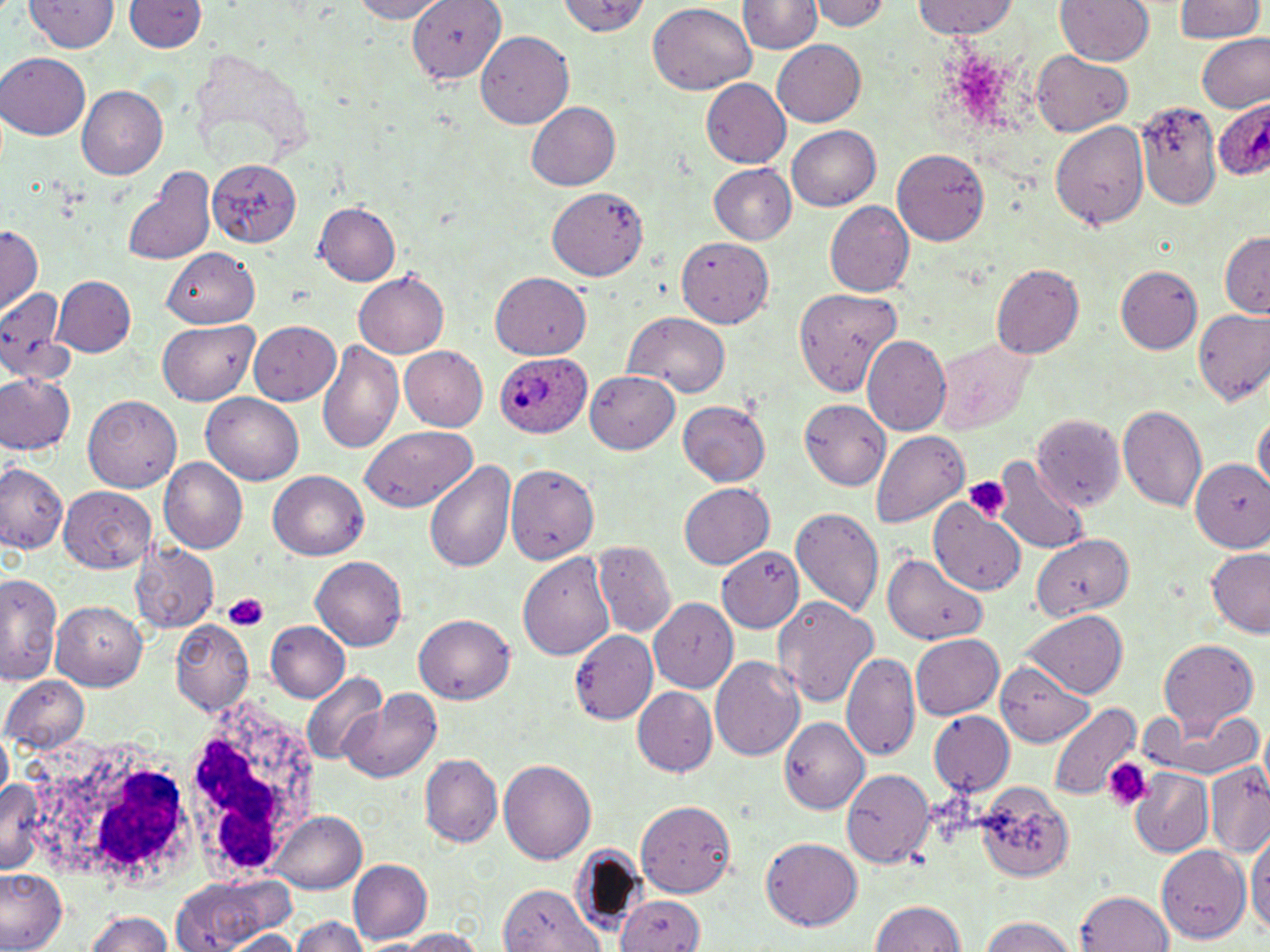

plasmodium_ovale_infected_red_blood_cell_locations: 'approximate bounding boxes as (x1, y1, x2, y2) in pixels: (1212, 99, 1270, 186), (486, 344, 590, 442)'
slide_level_diagnosis: Plasmodium ovale
magnification: 1000x
stain: May-Grünwald-Giemsa
preparation: thin blood film
uninfected_red_blood_cell_locations: 'approximate bounding boxes as (x1, y1, x2, y2) in pixels: (22, 0, 121, 54), (350, 0, 444, 22), (408, 0, 503, 82), (562, 0, 649, 41), (811, 0, 890, 30), (1055, 0, 1152, 66), (1172, 0, 1263, 43), (124, 1, 207, 55), (742, 1, 820, 56), (911, 1, 1024, 40), (1183, 2, 1263, 92), (645, 3, 757, 95), (480, 31, 575, 130), (1196, 34, 1270, 114), (771, 37, 867, 125), (1, 54, 90, 141), (1032, 54, 1132, 134), (702, 77, 791, 169), (77, 85, 167, 177), (1135, 100, 1223, 208), (526, 102, 620, 191), (1050, 118, 1151, 235), (785, 126, 881, 211), (893, 147, 991, 244), (209, 160, 301, 246), (123, 163, 218, 268), (707, 163, 797, 246), (551, 188, 646, 280), (825, 201, 913, 297), (314, 202, 401, 287), (0, 225, 42, 312), (1218, 231, 1270, 319), (676, 238, 776, 330), (164, 248, 258, 327), (992, 264, 1083, 360), (1117, 265, 1202, 357), (355, 270, 449, 356), (490, 274, 593, 359), (54, 275, 135, 354), (0, 286, 72, 380), (795, 288, 903, 398), (1191, 308, 1270, 405), (625, 310, 730, 395), (248, 320, 340, 402), (158, 322, 258, 403), (931, 334, 1035, 435), (862, 336, 950, 432), (318, 340, 403, 451), (397, 345, 487, 433), (584, 371, 681, 454), (0, 372, 75, 455), (202, 392, 306, 485), (84, 396, 182, 492), (801, 399, 891, 490), (675, 400, 772, 488), (1119, 404, 1209, 513), (1254, 415, 1269, 493), (360, 424, 480, 512), (869, 430, 970, 526), (424, 456, 517, 575), (159, 458, 246, 552), (990, 458, 1090, 556), (1190, 459, 1270, 553), (0, 460, 68, 557), (504, 460, 598, 565), (268, 472, 368, 561), (678, 483, 773, 569), (60, 487, 153, 574), (931, 501, 1028, 593), (789, 507, 883, 614), (1031, 533, 1132, 622), (593, 541, 674, 637), (132, 545, 218, 632), (721, 548, 804, 633), (1204, 549, 1270, 637), (518, 550, 617, 661), (885, 551, 989, 647), (311, 557, 407, 650), (1, 571, 60, 685), (772, 597, 878, 709), (651, 600, 738, 691), (52, 601, 147, 689), (1018, 610, 1130, 698), (417, 613, 516, 703), (169, 622, 255, 715), (265, 622, 352, 702), (568, 631, 659, 722), (909, 634, 1006, 720), (1158, 638, 1261, 735), (843, 653, 921, 765), (709, 655, 805, 764), (997, 668, 1098, 747), (300, 671, 387, 764), (3, 675, 89, 752), (631, 687, 717, 776), (341, 690, 442, 783), (1049, 701, 1141, 803), (1148, 707, 1264, 784), (932, 712, 1014, 798), (780, 717, 869, 813), (424, 754, 503, 847), (498, 758, 595, 863), (1204, 761, 1270, 854), (841, 767, 934, 867), (1129, 768, 1214, 856), (974, 778, 1072, 883), (638, 800, 738, 897), (272, 810, 366, 894), (1249, 825, 1269, 943), (761, 837, 864, 932), (1155, 845, 1249, 943), (347, 860, 431, 946), (0, 868, 67, 952), (171, 876, 288, 952), (499, 881, 598, 951), (1076, 890, 1174, 952), (614, 893, 704, 952), (868, 899, 969, 952), (84, 910, 179, 952), (974, 915, 1079, 952), (290, 917, 368, 952), (386, 927, 491, 952), (224, 931, 305, 952)'
image_size: 1270×952 pixels
platelet_locations: 'approximate bounding boxes as (x1, y1, x2, y2) in pixels: (964, 477, 1009, 522), (224, 593, 267, 629), (1105, 758, 1151, 812)'
modality: light microscopy
field_of_view: one of a larger specimen
white_blood_cell_locations: 'approximate bounding boxes as (x1, y1, x2, y2) in pixels: (168, 698, 320, 884), (22, 729, 213, 891)'